Report the malaria status of this cell.
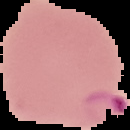
Parasitized.

Summary:
  - Image type: segmented cell region with the area outside set to black
  - Preparation: thin blood smear
  - Image size: 130×130 pixels